Describe the morphology of the red blood cells.
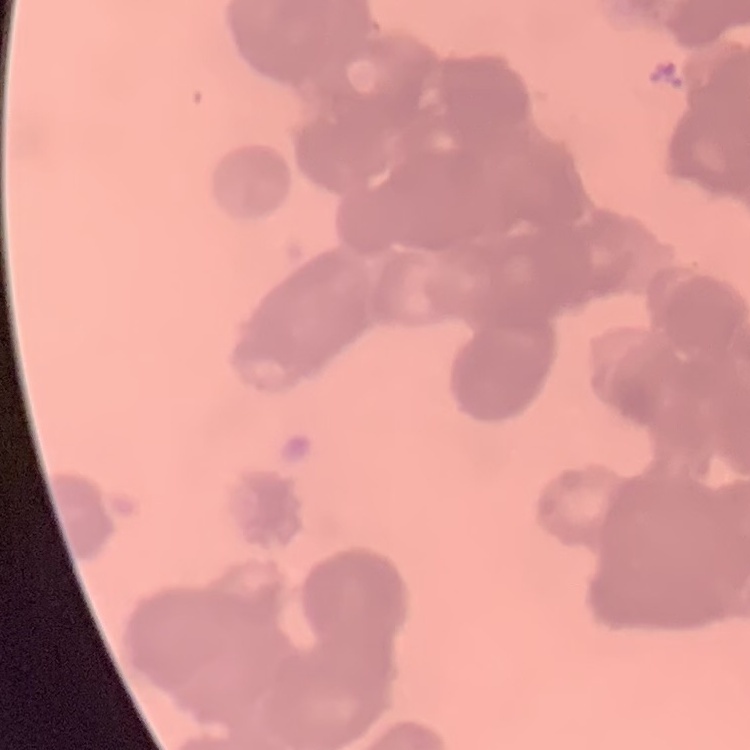
They show rouleaux formation.

Summary:
  - Image type: one tile cut from a larger photomicrograph
  - Stain: Field's or Giemsa
  - Preparation: thin blood film